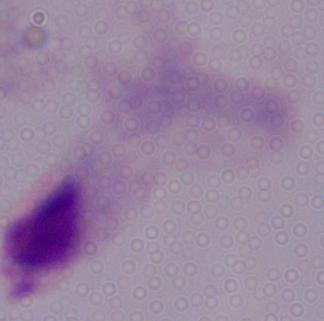
Summary:
  - Magnification: 1000x
  - Modality: photomicrograph
  - Identification: trichomonad